Report the malaria status of this cell.
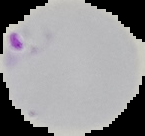

Parasitized.

From a thin blood smear. Cell region segmented out of the field of view; the surrounding area is masked to black. Image is 145×136 pixels.